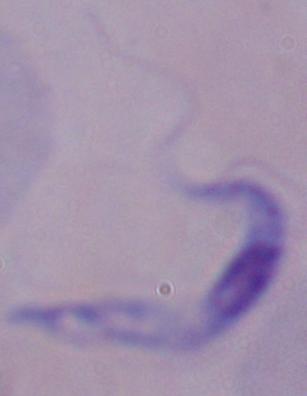

Summary:
  - Magnification: 1000x
  - Identification: trypanosome
  - Modality: photomicrograph